Name the blood parasite species.
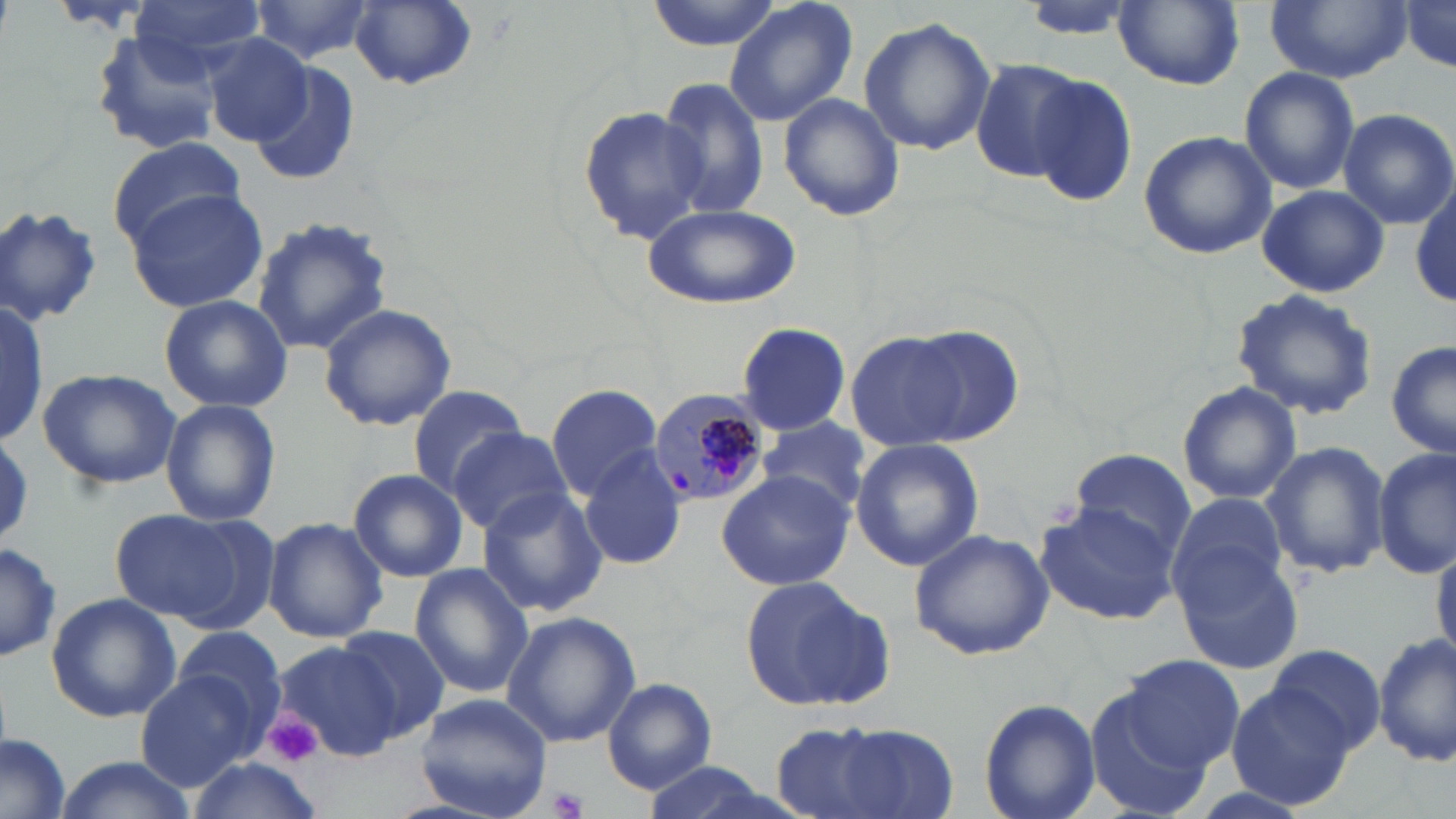
Plasmodium malariae.

uninfected red blood cell locations = approximate bounding boxes as (x1,y1)-(x2,y2) corner pairs in pixels: (129,0)-(265,68), (249,0)-(376,64), (647,0)-(781,51), (722,0)-(860,129), (1020,0)-(1132,43), (1264,0)-(1413,82), (348,1)-(477,90), (1113,1)-(1245,89), (1397,1)-(1456,77), (860,16)-(996,157), (88,31)-(225,157), (195,33)-(313,147), (972,59)-(1089,185), (249,61)-(360,188), (1240,66)-(1360,194), (1028,74)-(1138,205), (654,75)-(769,220), (779,93)-(904,221), (580,102)-(705,244), (1335,107)-(1456,229), (1138,130)-(1277,260), (106,140)-(246,246), (1256,184)-(1390,296), (1410,184)-(1456,309), (128,187)-(265,316), (643,203)-(801,309), (0,204)-(105,325), (249,216)-(396,356), (1232,287)-(1379,420), (159,294)-(293,412), (0,301)-(47,448), (317,304)-(457,431), (736,321)-(851,435), (890,325)-(1025,446), (845,333)-(971,452), (1387,341)-(1455,461), (37,368)-(183,489), (1177,382)-(1302,506), (405,384)-(528,498), (545,384)-(664,500), (161,397)-(282,528), (757,415)-(873,517), (448,427)-(573,534), (851,439)-(985,573), (1261,442)-(1391,580), (1069,446)-(1199,563), (1374,446)-(1455,578), (579,448)-(687,570), (348,469)-(470,583), (716,469)-(855,591), (477,482)-(607,620), (1168,490)-(1288,606), (1036,500)-(1180,624), (110,508)-(247,623), (264,516)-(388,644), (909,528)-(1054,660), (0,540)-(60,664), (1431,544)-(1456,663), (1173,546)-(1307,676), (408,565)-(533,701), (740,575)-(892,713), (45,593)-(181,723), (502,612)-(640,747), (332,624)-(448,740), (171,629)-(290,734), (1372,631)-(1454,765), (274,641)-(411,761), (1270,645)-(1385,756), (1115,654)-(1246,774), (135,670)-(260,792), (603,679)-(717,793), (1227,681)-(1354,809), (1087,689)-(1209,814), (415,694)-(552,817), (979,698)-(1102,819), (770,715)-(956,816), (0,736)-(71,819), (60,757)-(193,817), (189,758)-(325,819), (637,761)-(787,819)
field of view = single
stain = May-Grünwald-Giemsa
image size = 1456×819 pixels
platelet locations = approximate bounding boxes as (x1,y1)-(x2,y2) corner pairs in pixels: (267,716)-(323,767), (551,788)-(586,817)
preparation = thin blood smear
Plasmodium malariae-infected red blood cell locations = approximate bounding boxes as (x1,y1)-(x2,y2) corner pairs in pixels: (648,390)-(773,507)
modality = light microscopy
magnification = 1000x